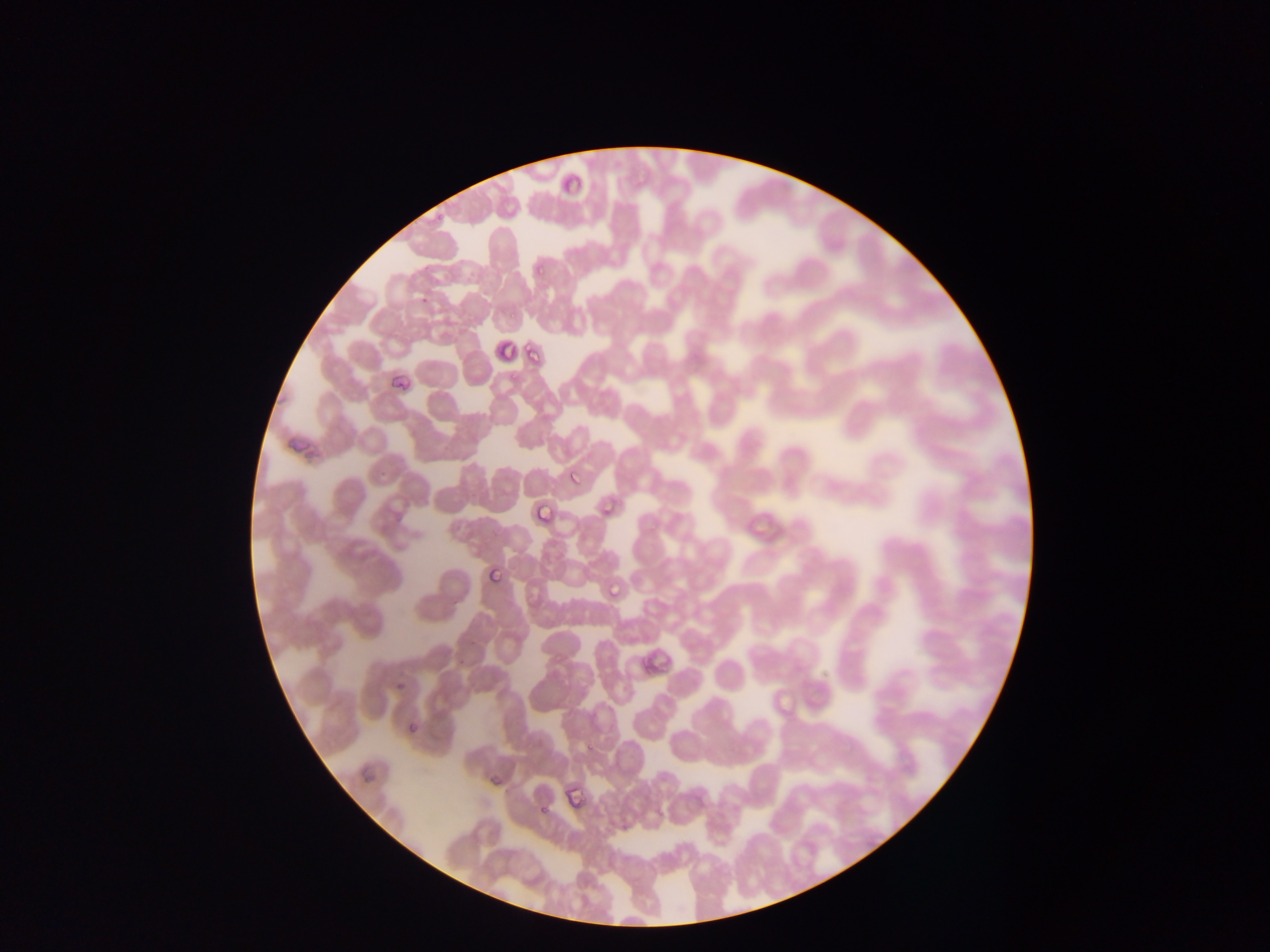

Approximate bounding boxes as [left, top, right, bottom] in pixels. Malaria parasite locations: [534, 259, 554, 276], [419, 291, 436, 309], [511, 310, 518, 321], [498, 341, 515, 360], [528, 344, 542, 364], [506, 371, 519, 386], [389, 373, 407, 390], [564, 464, 583, 492], [601, 497, 622, 518], [533, 501, 556, 528], [484, 568, 505, 586], [607, 577, 626, 597], [394, 674, 412, 694], [404, 713, 419, 742], [585, 740, 596, 756]. Thin blood film. Single field of view. Image is 1270×952 pixels. Collected in Ghana. Mobile-phone photograph taken through the microscope.